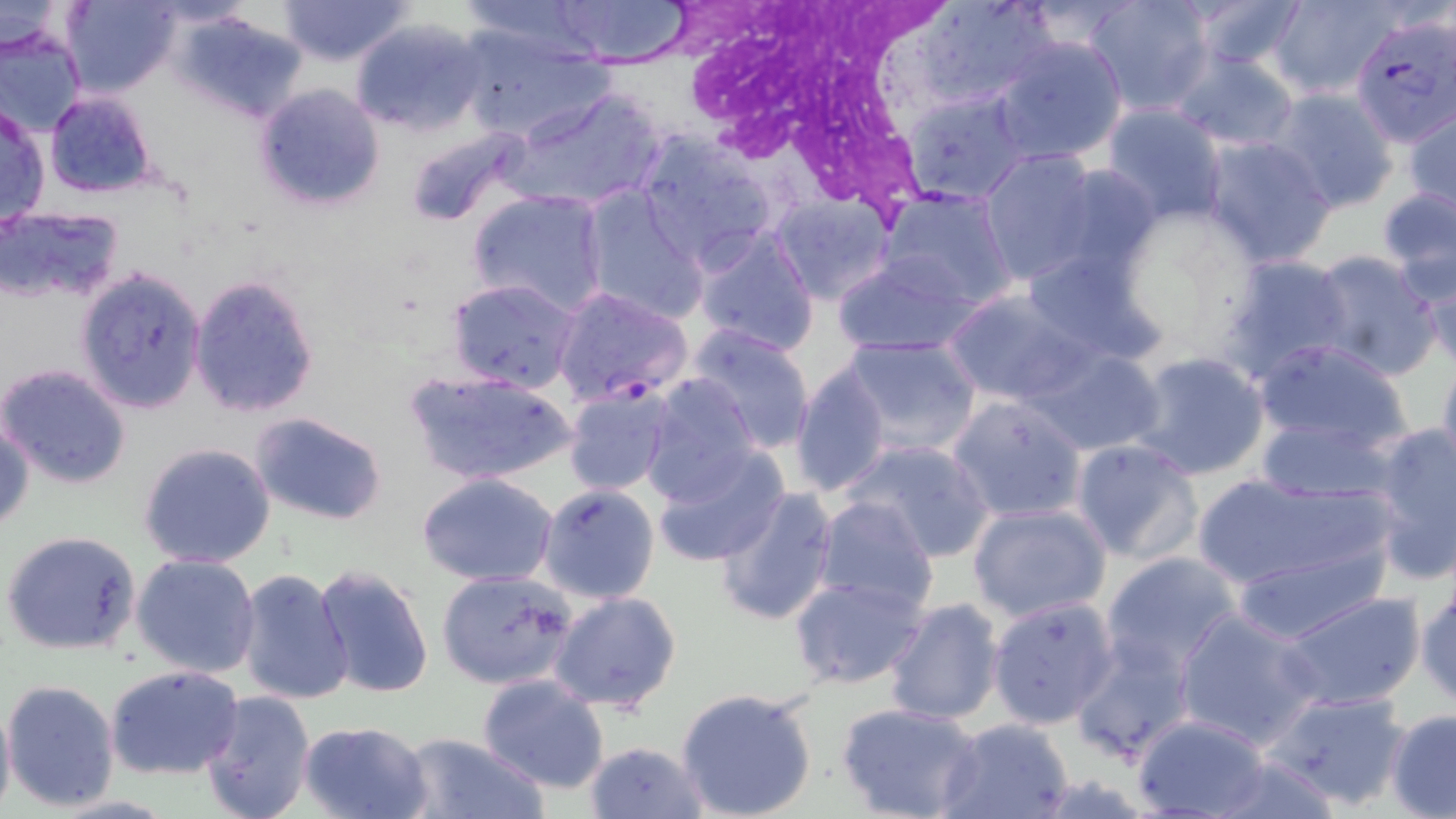
{
  "slide_level_diagnosis": "Plasmodium falciparum",
  "uninfected_red_blood_cell_locations": "approximate bounding boxes as (x1, y1, x2, y2) in pixels: (63, 0, 181, 98), (278, 0, 411, 66), (551, 0, 694, 68), (913, 0, 1055, 111), (1083, 0, 1215, 115), (1183, 0, 1312, 75), (1265, 0, 1402, 101), (0, 1, 85, 60), (173, 9, 309, 123), (349, 17, 488, 137), (454, 26, 611, 144), (0, 27, 87, 141), (990, 36, 1128, 166), (1168, 49, 1301, 152), (252, 83, 386, 212), (506, 86, 666, 212), (1269, 88, 1399, 213), (902, 90, 1030, 204), (44, 91, 158, 200), (1100, 103, 1231, 227), (0, 104, 50, 227), (1404, 107, 1456, 216), (402, 125, 531, 230), (634, 130, 779, 270), (1201, 136, 1338, 268), (975, 150, 1103, 286), (1044, 164, 1165, 278), (579, 185, 709, 324), (878, 185, 1018, 310), (1376, 187, 1456, 300), (469, 188, 609, 317), (769, 194, 895, 307), (1, 206, 126, 304), (1108, 206, 1264, 359), (690, 225, 821, 355), (1021, 246, 1166, 365), (834, 250, 984, 357), (1305, 251, 1443, 381), (1414, 252, 1455, 371), (1218, 254, 1356, 384), (74, 267, 207, 415), (189, 273, 320, 418), (445, 277, 580, 392), (942, 288, 1095, 406), (686, 324, 815, 455), (836, 335, 983, 458), (1252, 338, 1416, 456), (1025, 343, 1166, 456), (1126, 349, 1274, 482), (1435, 351, 1456, 478), (789, 360, 893, 498), (0, 362, 131, 487), (405, 368, 579, 487), (638, 373, 765, 505), (563, 382, 677, 497), (948, 394, 1088, 525), (1, 412, 35, 535), (249, 412, 389, 526), (1258, 415, 1401, 501), (1367, 425, 1456, 583), (1070, 438, 1204, 565), (844, 439, 995, 561), (138, 442, 277, 569), (652, 445, 788, 567), (1193, 471, 1397, 602), (418, 473, 559, 587), (537, 484, 661, 604), (713, 488, 839, 625), (813, 497, 939, 616), (967, 502, 1111, 622), (2, 529, 142, 655), (1230, 542, 1382, 644), (1100, 551, 1244, 676), (132, 553, 260, 679), (313, 563, 436, 703), (234, 567, 356, 706), (436, 569, 577, 690), (1415, 572, 1456, 711), (790, 575, 929, 689), (549, 590, 682, 713), (1278, 591, 1428, 712), (983, 593, 1118, 729), (880, 595, 1004, 724), (1173, 609, 1324, 749), (1068, 636, 1194, 763), (105, 664, 246, 781), (477, 672, 610, 793), (2, 678, 120, 811), (675, 686, 818, 819), (1264, 689, 1412, 811), (0, 690, 16, 819), (198, 690, 317, 819), (836, 702, 983, 819), (1386, 709, 1456, 818), (1130, 713, 1275, 819), (936, 717, 1076, 819), (298, 720, 435, 819), (397, 731, 549, 819), (584, 740, 707, 819), (1201, 753, 1345, 819)",
  "plasmodium_falciparum_infected_red_blood_cell_locations": "approximate bounding boxes as (x1, y1, x2, y2) in pixels: (1349, 10, 1455, 146), (550, 285, 692, 407)",
  "image_size": "1456×819 pixels",
  "field_of_view": "one of a larger specimen",
  "white_blood_cell_locations": "approximate bounding boxes as (x1, y1, x2, y2) in pixels: (693, 1, 957, 202)",
  "stain": "May-Grünwald-Giemsa",
  "preparation": "thin blood film",
  "modality": "optical microscopy",
  "magnification": "1000x"
}